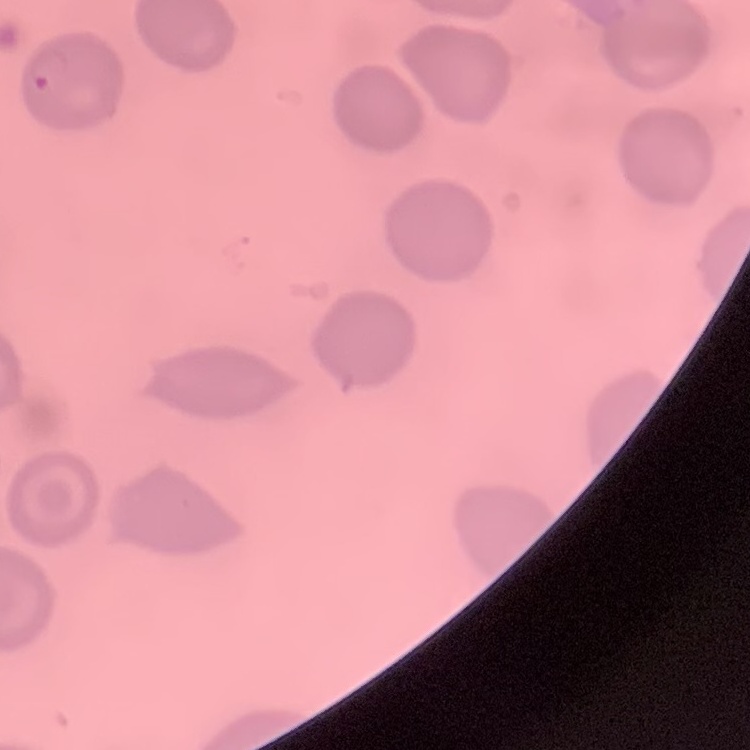
The erythrocytes exhibit no rouleaux formation. Thin blood film. Field's or Giemsa stain. One tile cut from a larger photomicrograph.